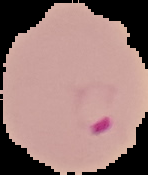

{
  "image_type": "cell region segmented out of the field of view; surrounding area masked to black",
  "preparation": "thin blood smear",
  "result": "Plasmodium parasites detected",
  "image_size": "148×175 pixels"
}